Outline each uninfected red blood cell.
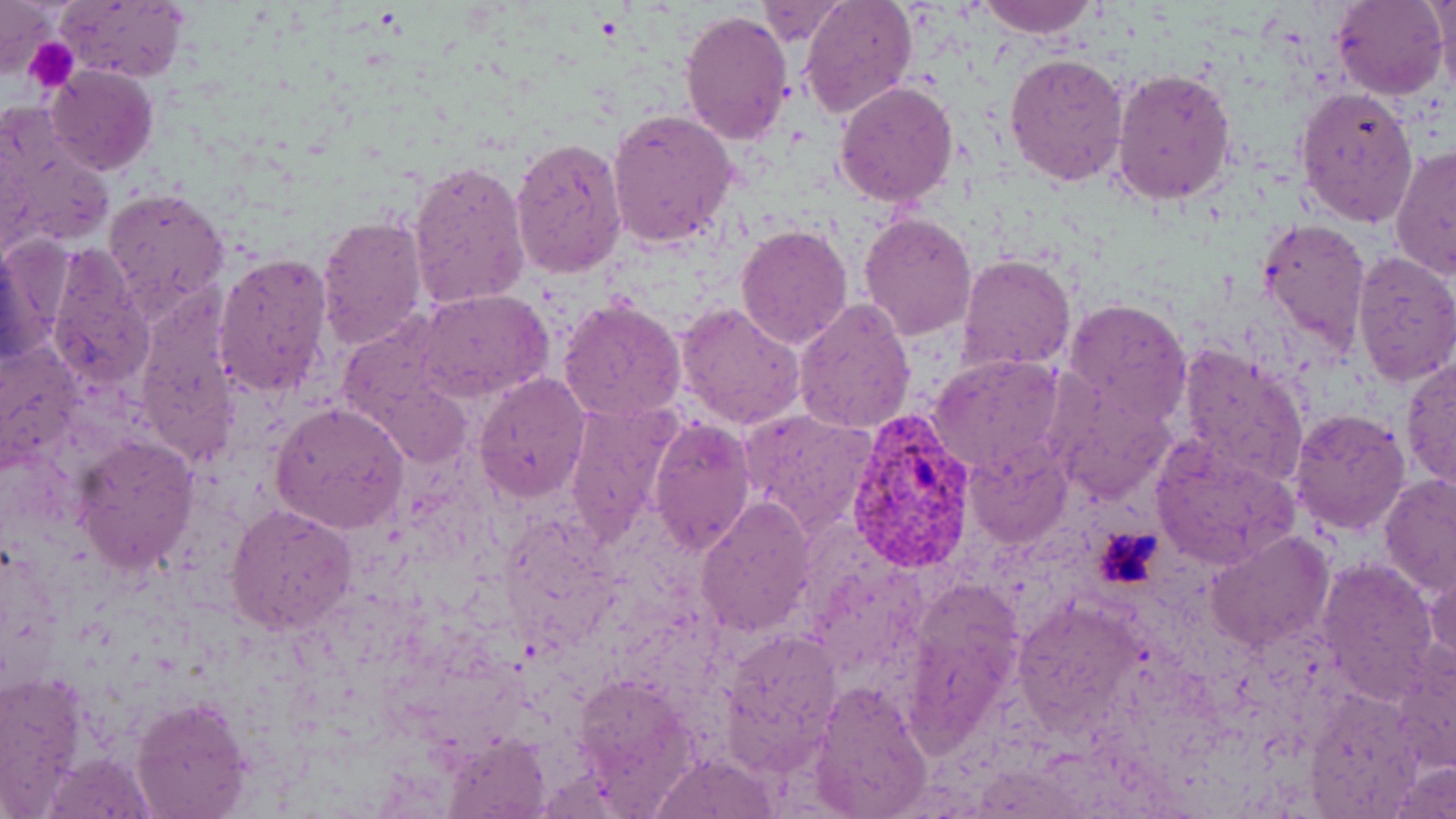
Approximate bounding boxes as named x1/y1/x2/y2 corners in pixels.
Uninfected red blood cells: (x1=800, y1=0, x2=919, y2=119), (x1=977, y1=0, x2=1097, y2=38), (x1=1332, y1=0, x2=1450, y2=101), (x1=1432, y1=0, x2=1456, y2=89), (x1=0, y1=1, x2=56, y2=78), (x1=55, y1=2, x2=189, y2=82), (x1=756, y1=4, x2=848, y2=46), (x1=680, y1=10, x2=793, y2=145), (x1=1004, y1=52, x2=1130, y2=187), (x1=44, y1=65, x2=159, y2=178), (x1=1111, y1=67, x2=1237, y2=205), (x1=834, y1=79, x2=960, y2=207), (x1=1295, y1=85, x2=1418, y2=229), (x1=606, y1=109, x2=737, y2=249), (x1=3, y1=119, x2=114, y2=257), (x1=510, y1=137, x2=627, y2=278), (x1=1390, y1=145, x2=1456, y2=282), (x1=405, y1=160, x2=529, y2=313), (x1=104, y1=187, x2=229, y2=315), (x1=859, y1=211, x2=977, y2=340), (x1=316, y1=214, x2=428, y2=353), (x1=1259, y1=216, x2=1372, y2=362), (x1=735, y1=224, x2=853, y2=350), (x1=1, y1=240, x2=53, y2=367), (x1=44, y1=251, x2=153, y2=388), (x1=213, y1=251, x2=332, y2=401), (x1=1351, y1=252, x2=1456, y2=386), (x1=956, y1=253, x2=1076, y2=375), (x1=416, y1=289, x2=552, y2=400), (x1=792, y1=296, x2=915, y2=433), (x1=558, y1=298, x2=687, y2=424), (x1=1064, y1=298, x2=1192, y2=425), (x1=676, y1=301, x2=804, y2=429), (x1=137, y1=312, x2=238, y2=456), (x1=431, y1=315, x2=572, y2=468), (x1=338, y1=326, x2=467, y2=455), (x1=0, y1=340, x2=82, y2=465), (x1=1177, y1=344, x2=1309, y2=486), (x1=929, y1=352, x2=1068, y2=477), (x1=1403, y1=355, x2=1456, y2=488), (x1=474, y1=374, x2=591, y2=502), (x1=1051, y1=380, x2=1176, y2=503), (x1=561, y1=399, x2=685, y2=547), (x1=272, y1=403, x2=409, y2=533), (x1=1290, y1=407, x2=1412, y2=534), (x1=741, y1=408, x2=879, y2=534), (x1=648, y1=416, x2=756, y2=556), (x1=72, y1=433, x2=199, y2=575), (x1=1150, y1=442, x2=1300, y2=568), (x1=965, y1=447, x2=1072, y2=550), (x1=1380, y1=475, x2=1456, y2=596), (x1=695, y1=496, x2=816, y2=637), (x1=226, y1=506, x2=356, y2=633), (x1=1205, y1=530, x2=1334, y2=651), (x1=1315, y1=556, x2=1441, y2=700), (x1=1426, y1=567, x2=1456, y2=675), (x1=904, y1=578, x2=1026, y2=738), (x1=1014, y1=600, x2=1143, y2=730), (x1=724, y1=630, x2=841, y2=764), (x1=0, y1=673, x2=88, y2=813), (x1=808, y1=680, x2=933, y2=818), (x1=1306, y1=691, x2=1427, y2=815), (x1=131, y1=696, x2=251, y2=819), (x1=444, y1=736, x2=549, y2=816), (x1=651, y1=755, x2=774, y2=817), (x1=1391, y1=760, x2=1454, y2=818).

{
  "slide_level_diagnosis": "Plasmodium vivax",
  "image_size": "1456×819 pixels",
  "stain": "May-Grünwald-Giemsa",
  "plasmodium_vivax_infected_red_blood_cell_locations": "approximate bounding boxes as named x1/y1/x2/y2 corners in pixels: (x1=845, y1=411, x2=979, y2=574)",
  "platelet_locations": "approximate bounding boxes as named x1/y1/x2/y2 corners in pixels: (x1=28, y1=40, x2=79, y2=92), (x1=1093, y1=526, x2=1163, y2=588)",
  "magnification": "1000x",
  "preparation": "thin blood film",
  "field_of_view": "single",
  "modality": "optical microscopy"
}